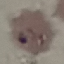
Result: malaria parasites detected. Thin blood film. Giemsa-stained preparation. Acquired by smartphone through the microscope eyepiece. Cell patch, automatically extracted from a larger field of view and resized to 64 × 64 pixels.